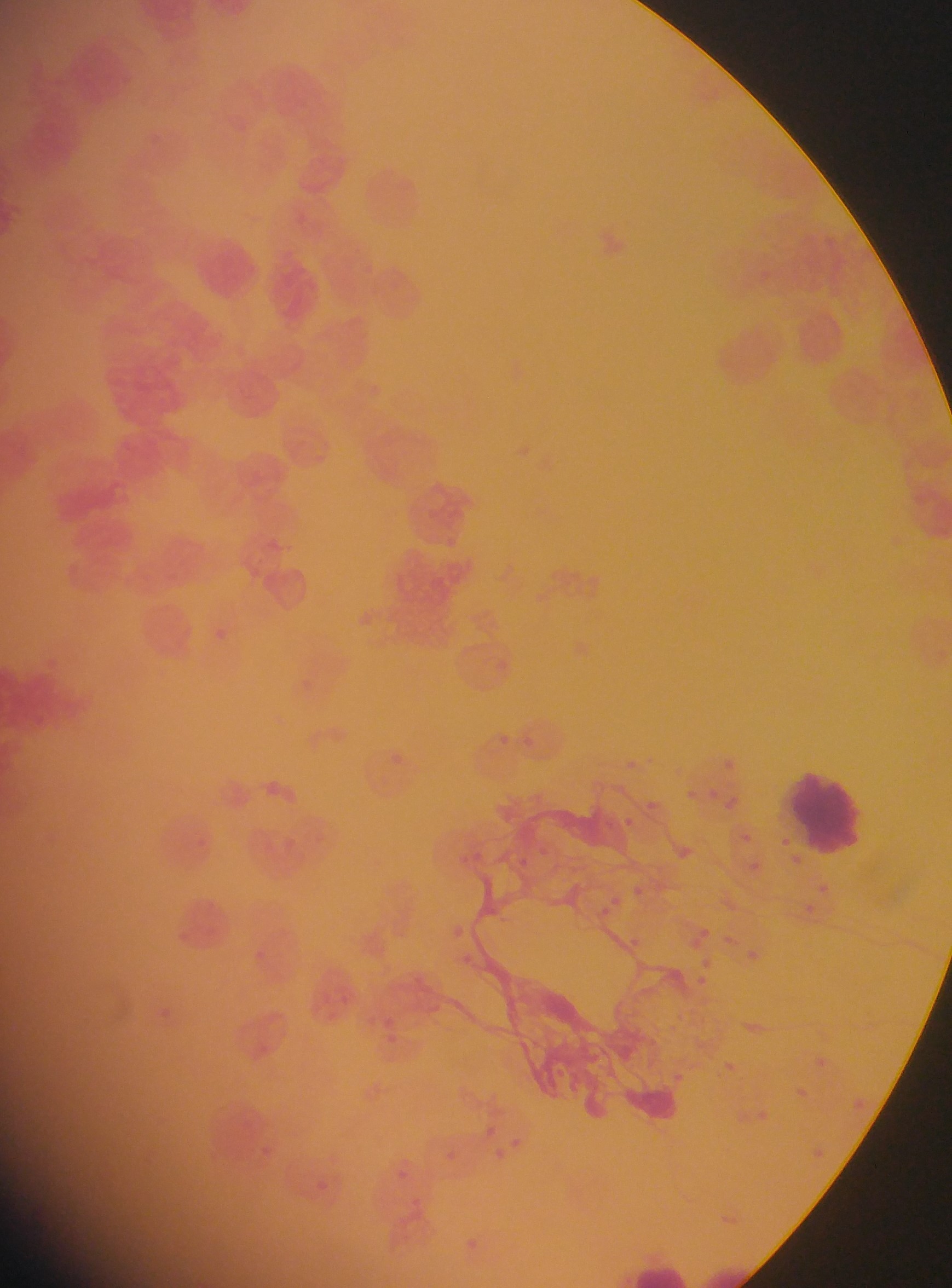
Approximate bounding boxes as (left, top, right, bottom) in pixels.
Summary:
  - Plasmodium parasite locations: (347, 603, 372, 636), (208, 621, 224, 648), (497, 725, 513, 748), (391, 746, 419, 779), (718, 756, 734, 770), (622, 759, 638, 771), (260, 775, 285, 800), (711, 784, 725, 806), (639, 796, 661, 818), (616, 812, 639, 835), (734, 829, 753, 848), (678, 842, 692, 858), (515, 849, 536, 876), (746, 854, 769, 876), (812, 879, 832, 899), (601, 888, 633, 918), (702, 921, 720, 947), (628, 932, 640, 947), (740, 944, 764, 966), (461, 949, 475, 965), (683, 955, 723, 996), (384, 1011, 407, 1053), (807, 1053, 829, 1072), (718, 1057, 738, 1072), (669, 1062, 685, 1084), (791, 1083, 814, 1105), (855, 1094, 877, 1120), (478, 1121, 496, 1135), (814, 1132, 830, 1165), (487, 1140, 517, 1167), (448, 1142, 460, 1160), (407, 1190, 422, 1206), (463, 1223, 491, 1256)
  - Leukocyte locations: (193, 235, 265, 305), (789, 767, 869, 858), (621, 1253, 690, 1288)
  - Country: Ghana
  - Image size: 952×1288 pixels
  - Field of view: single
  - Preparation: thin blood film
  - Capture: mobile-phone photograph through a microscope